Classify this cell by malaria status.
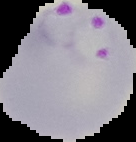

Parasitized.

Image is 136×142 pixels. From a thin blood film. Cell region segmented out of the field of view; the surrounding area is masked to black.